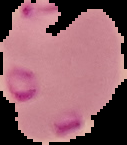 Result: Plasmodium parasites detected. Image is 127×145 pixels. From a thin blood smear. Segmented cell region on a black background.